Assess this cell for malaria.
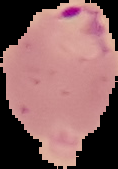
Parasitized.

image type = cell region segmented out of the field of view; surrounding area masked to black
image size = 118×169 pixels
preparation = thin blood smear